Report the malaria status of this cell.
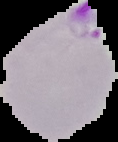
It is parasitized.

From a thin blood film. Segmented cell region on a black background. Image is 118×142 pixels.